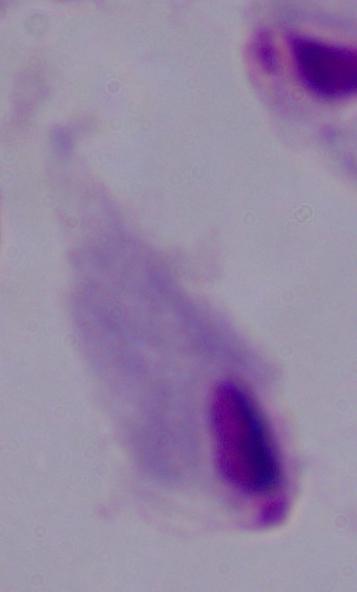

Summary:
  - Identification: trichomonad
  - Magnification: 1000x
  - Modality: micrograph